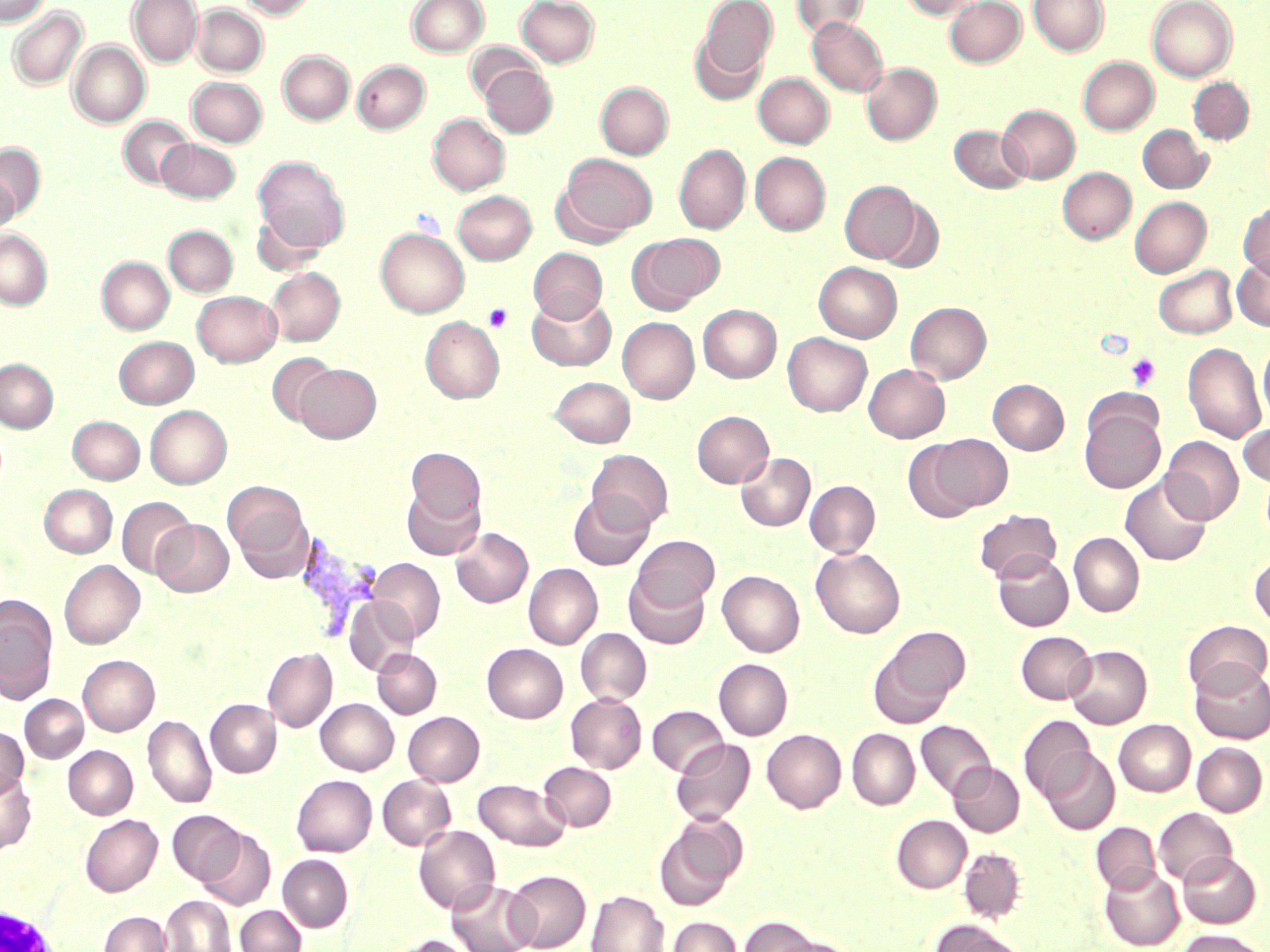

Approximate bounding boxes as [x1, y1, x2, y2] in pixels. Uninfected red blood cell locations: [0, 0, 49, 26], [127, 0, 203, 67], [238, 0, 317, 19], [407, 0, 488, 56], [517, 0, 599, 67], [697, 0, 777, 81], [792, 0, 867, 39], [900, 0, 984, 19], [945, 0, 1025, 67], [1029, 0, 1108, 56], [1147, 0, 1237, 81], [192, 4, 267, 76], [7, 7, 87, 90], [807, 17, 888, 96], [690, 32, 768, 106], [68, 41, 150, 128], [466, 41, 539, 103], [278, 51, 354, 125], [1078, 57, 1158, 134], [353, 60, 429, 133], [861, 63, 941, 145], [480, 64, 556, 137], [754, 72, 834, 148], [187, 77, 267, 146], [1188, 77, 1254, 144], [596, 82, 673, 159], [998, 104, 1080, 183], [428, 112, 509, 195], [119, 116, 194, 189], [1138, 124, 1212, 193], [950, 125, 1030, 193], [157, 138, 239, 202], [1, 143, 45, 218], [674, 144, 750, 234], [750, 152, 830, 235], [557, 153, 657, 240], [253, 157, 350, 253], [1057, 167, 1135, 244], [0, 172, 18, 236], [839, 180, 921, 263], [453, 190, 536, 264], [873, 196, 945, 273], [1130, 196, 1211, 277], [1238, 201, 1270, 279], [251, 211, 325, 277], [163, 225, 237, 297], [376, 228, 469, 317], [0, 229, 52, 310], [628, 233, 724, 312], [529, 247, 607, 322], [1232, 255, 1270, 330], [97, 257, 173, 334], [814, 262, 902, 342], [1153, 265, 1236, 338], [265, 267, 345, 345], [193, 290, 281, 366], [527, 291, 615, 371], [905, 301, 991, 383], [698, 304, 781, 382], [420, 316, 504, 402], [617, 317, 699, 403], [782, 333, 872, 415], [115, 336, 198, 408], [1258, 337, 1270, 426], [1182, 342, 1267, 445], [266, 352, 338, 427], [0, 358, 58, 432], [294, 364, 380, 442], [864, 364, 949, 442], [549, 376, 635, 447], [988, 379, 1068, 454], [145, 405, 231, 489], [692, 410, 774, 488], [1080, 410, 1165, 493], [68, 416, 144, 484], [1238, 422, 1270, 487], [934, 434, 1012, 511], [1162, 436, 1243, 523], [903, 439, 986, 524], [406, 447, 486, 527], [586, 449, 673, 530], [736, 452, 815, 531], [1120, 473, 1212, 567], [805, 480, 880, 557], [402, 483, 485, 559], [39, 484, 117, 558], [226, 485, 312, 580], [569, 489, 655, 570], [117, 497, 196, 579], [973, 509, 1062, 583], [152, 519, 233, 597], [451, 527, 533, 607], [1069, 532, 1144, 617], [632, 535, 719, 609], [811, 548, 905, 638], [993, 550, 1074, 631], [1249, 552, 1270, 629], [368, 559, 444, 642], [59, 560, 144, 649], [524, 563, 602, 649], [624, 568, 710, 649], [717, 570, 804, 656], [0, 594, 57, 701], [344, 596, 418, 677], [1184, 620, 1269, 696], [576, 628, 651, 705], [869, 628, 968, 727], [1016, 631, 1095, 704], [482, 643, 568, 723], [1065, 645, 1151, 728], [263, 648, 337, 732], [373, 648, 441, 718], [78, 655, 160, 735], [714, 659, 792, 740], [1189, 660, 1270, 744], [566, 694, 647, 772], [20, 695, 87, 762], [206, 699, 281, 777], [315, 699, 398, 774], [647, 705, 729, 776], [403, 711, 485, 785], [143, 714, 216, 808], [1019, 715, 1095, 801], [916, 720, 996, 800], [1114, 720, 1195, 796], [0, 727, 28, 798], [762, 729, 846, 812], [847, 729, 920, 809], [671, 738, 755, 825], [1192, 742, 1268, 816], [64, 746, 137, 818], [1041, 748, 1120, 834], [949, 761, 1025, 836], [539, 762, 616, 831], [0, 771, 35, 855], [292, 775, 377, 856], [377, 776, 455, 850], [473, 778, 570, 851], [1154, 808, 1237, 885], [168, 809, 244, 885], [80, 814, 162, 896], [655, 814, 747, 911], [892, 815, 971, 892], [1091, 822, 1161, 894], [414, 825, 500, 914], [196, 828, 276, 910], [959, 848, 1026, 922], [1178, 851, 1261, 928], [278, 854, 354, 932], [1099, 867, 1185, 950], [505, 870, 590, 952], [447, 879, 537, 952], [587, 890, 669, 952], [161, 896, 235, 952], [235, 905, 306, 952], [98, 911, 172, 952], [737, 915, 820, 952], [668, 916, 742, 952], [931, 919, 1030, 952], [1175, 929, 1267, 952], [386, 934, 477, 952], [770, 936, 859, 952]. Plasmodium vivax-infected red blood cell locations: [294, 528, 383, 637]. Platelet locations: [484, 304, 512, 332], [1125, 353, 1160, 391]. Slide-level diagnosis: Plasmodium vivax. May-Grünwald-Giemsa-stained preparation. Image is 1270×952 pixels. Single field of view. Thin blood smear. 1000x magnification. Light microscopy.